Give the extent of all Trypanosoma brucei.
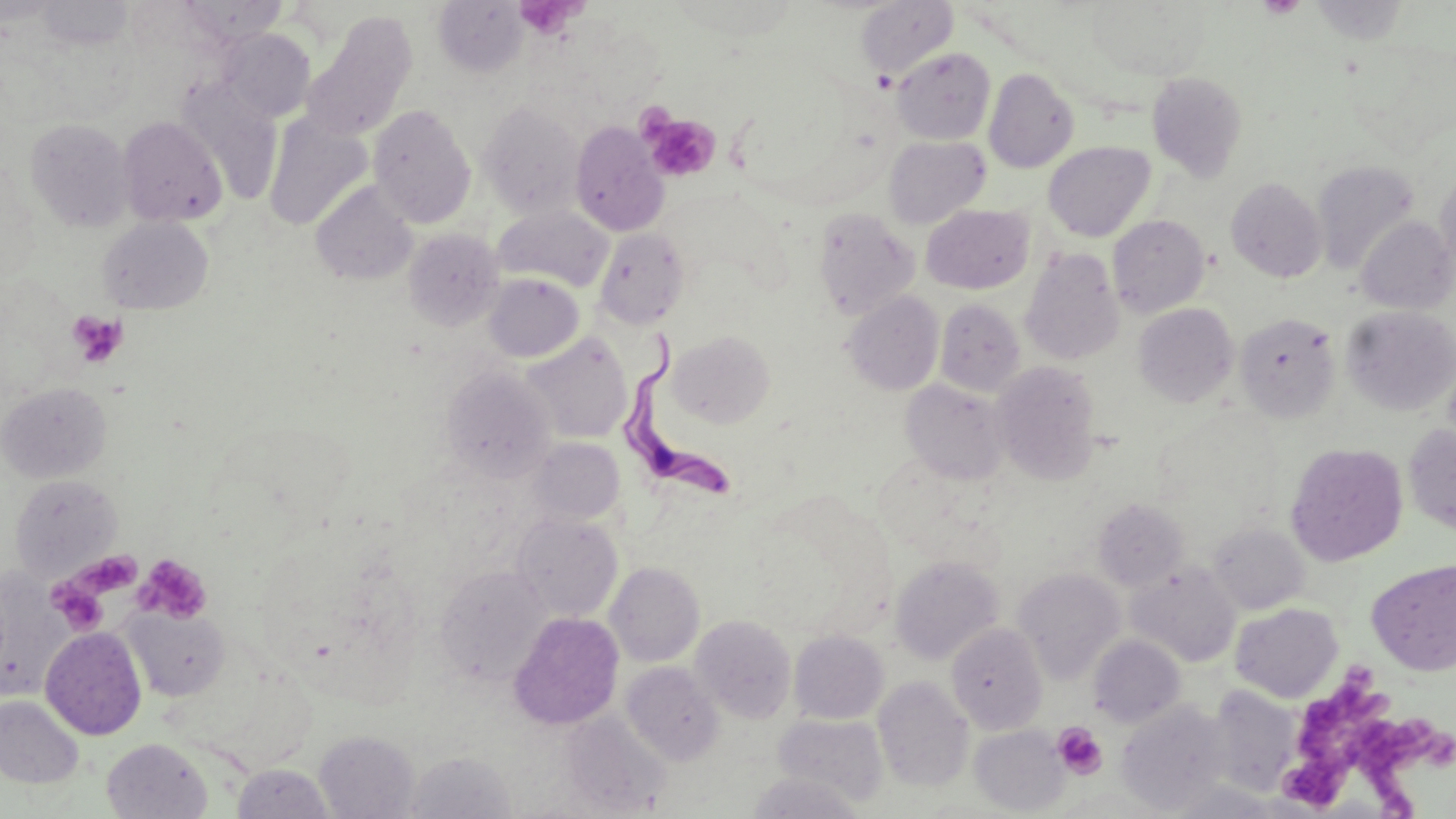
Approximate bounding boxes as [x1, y1, x2, y2] in pixels.
Trypanosoma brucei: [626, 332, 733, 507].

slide-level diagnosis = Trypanosoma brucei
stain = May-Grünwald-Giemsa
field of view = single
platelet locations = approximate bounding boxes as [x1, y1, x2, y2] in pixels: [1256, 0, 1307, 18], [515, 1, 581, 39], [640, 112, 721, 182], [66, 309, 127, 368], [77, 550, 142, 596], [133, 554, 212, 623], [50, 559, 123, 613], [49, 581, 109, 635], [1302, 660, 1398, 758], [1355, 714, 1456, 819], [1052, 722, 1107, 779], [1283, 746, 1365, 809]
uninfected red blood cell locations = approximate bounding boxes as [x1, y1, x2, y2] in pixels: [178, 0, 288, 46], [856, 0, 958, 83], [37, 1, 133, 49], [433, 1, 528, 78], [1088, 1, 1211, 81], [302, 13, 417, 140], [219, 28, 315, 122], [892, 48, 996, 144], [984, 68, 1079, 173], [1147, 72, 1247, 182], [175, 79, 284, 203], [477, 100, 585, 218], [368, 104, 476, 229], [264, 115, 372, 230], [117, 116, 227, 227], [25, 118, 134, 231], [570, 121, 669, 236], [884, 136, 990, 229], [1042, 141, 1155, 241], [1312, 161, 1419, 273], [1435, 171, 1456, 272], [1226, 177, 1327, 282], [311, 180, 418, 287], [922, 204, 1034, 294], [493, 206, 615, 293], [811, 208, 920, 321], [1108, 214, 1210, 318], [1356, 216, 1455, 314], [98, 217, 214, 314], [402, 228, 505, 332], [594, 228, 691, 329], [1020, 249, 1124, 365], [484, 273, 584, 362], [842, 291, 944, 396], [934, 298, 1025, 396], [1133, 302, 1238, 408], [1342, 306, 1456, 415], [1234, 312, 1341, 423], [669, 330, 775, 428], [522, 332, 633, 443], [991, 361, 1101, 484], [441, 365, 558, 481], [901, 379, 1009, 485], [0, 382, 111, 483], [1404, 424, 1456, 535], [529, 437, 625, 525], [1284, 442, 1409, 566], [9, 473, 122, 579], [1092, 498, 1188, 591], [511, 512, 623, 623], [1208, 522, 1309, 614], [890, 556, 1004, 665], [1367, 559, 1456, 676], [1126, 561, 1241, 667], [605, 562, 705, 667], [434, 564, 553, 686], [1012, 568, 1126, 685], [0, 573, 69, 701], [1230, 603, 1343, 703], [122, 606, 231, 702], [508, 611, 625, 730], [691, 614, 797, 723], [946, 622, 1047, 734], [40, 626, 147, 740], [789, 630, 888, 724], [1087, 635, 1186, 728], [620, 660, 724, 766], [873, 675, 973, 792], [1206, 685, 1304, 796], [0, 695, 84, 788], [1117, 700, 1232, 814], [560, 710, 671, 817], [772, 714, 890, 808], [969, 724, 1069, 815], [314, 730, 420, 819], [102, 737, 212, 819], [405, 751, 516, 819], [232, 763, 335, 818], [746, 772, 865, 818], [1165, 781, 1291, 818]
preparation = thin blood smear
image size = 1456×819 pixels
magnification = 1000x
modality = optical microscopy